Assess for malaria.
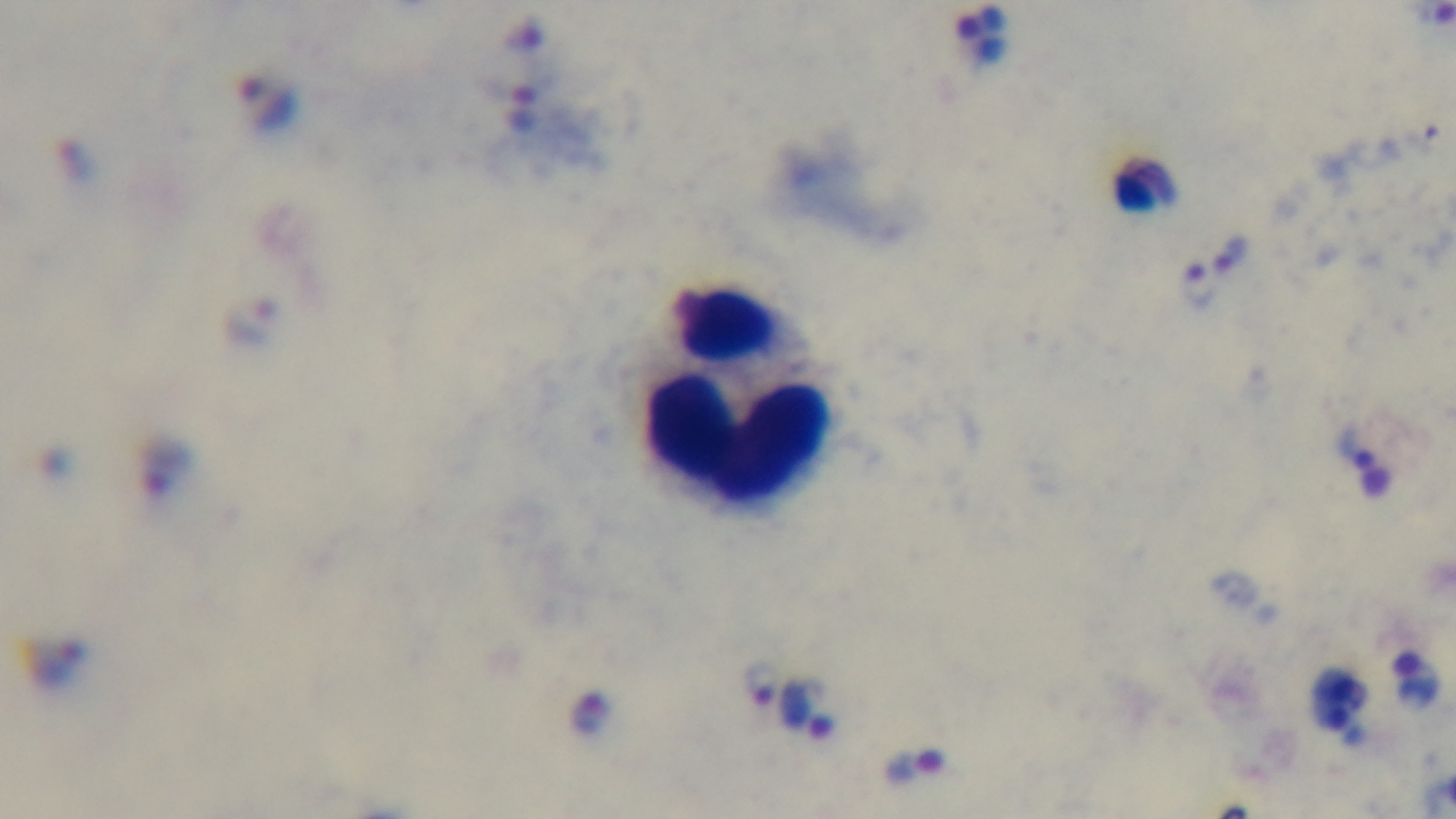
Infected.

Summary:
  - Stain: Giemsa
  - Field of view: one from the slide
  - Modality: light microscopy
  - Preparation: thick blood film
  - Capture: mounted 4K digital camera
  - Objective: 100x oil immersion